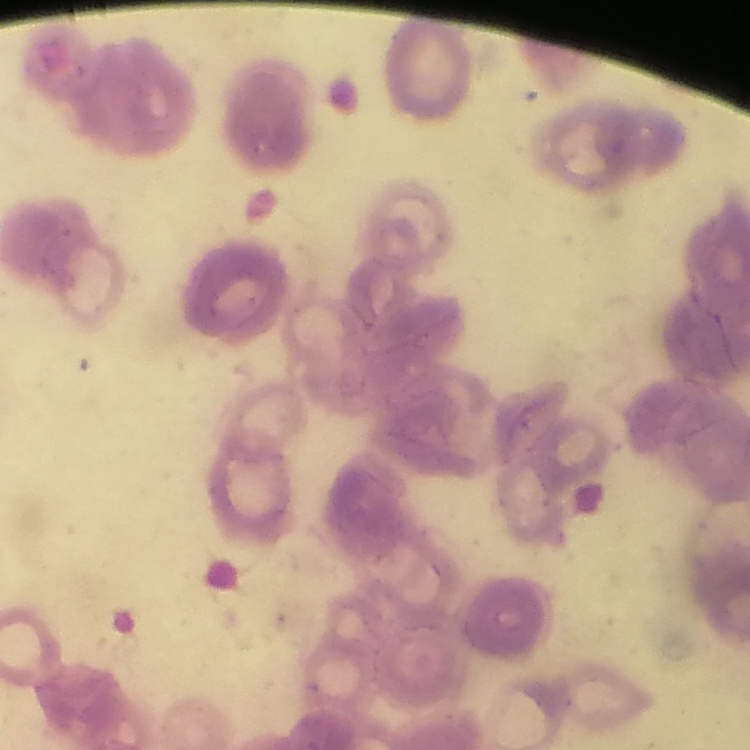
Summary:
  - Erythrocyte morphology: rouleaux formation
  - Preparation: thin blood film
  - Stain: Field's or Giemsa
  - Image type: one tile cut from a larger photomicrograph